Describe the morphology of the erythrocytes.
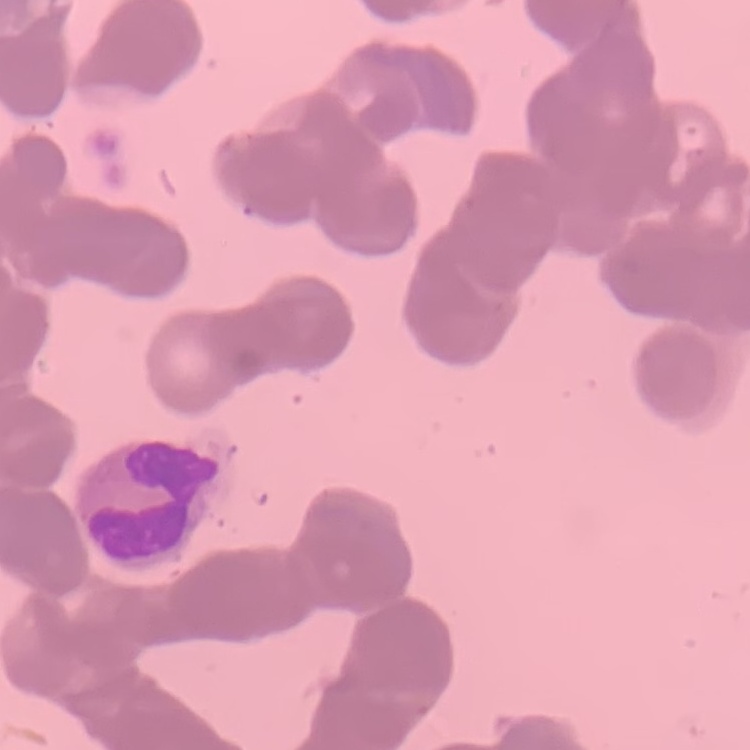

Rouleaux formation.

Thin blood smear. Square crop of a larger photomicrograph. Stained with either Field's or Giemsa.